Locate and identify every blood parasite.
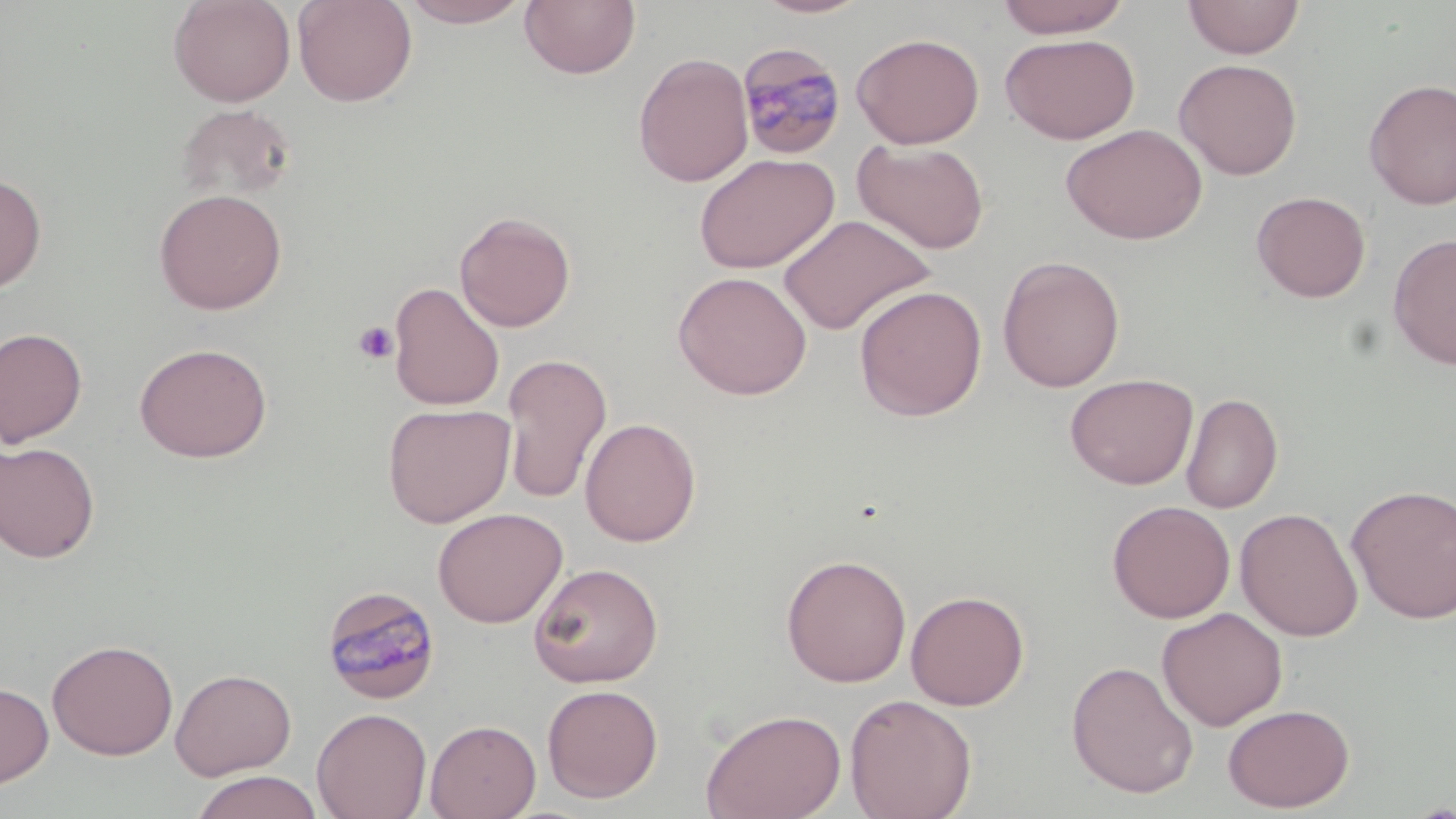

Approximate bounding boxes as named x1/y1/x2/y2 corners in pixels.
Plasmodium malariae-infected red blood cells: (x1=736, y1=42, x2=847, y2=161), (x1=321, y1=585, x2=440, y2=705).
No Plasmodium falciparum, Plasmodium ovale, Plasmodium vivax, Babesia divergens, or Trypanosoma brucei observed.

Summary:
  - Platelet locations: (x1=352, y1=320, x2=398, y2=365)
  - Uninfected red blood cell locations: (x1=168, y1=0, x2=296, y2=106), (x1=292, y1=0, x2=418, y2=107), (x1=398, y1=0, x2=534, y2=28), (x1=519, y1=0, x2=640, y2=80), (x1=752, y1=0, x2=874, y2=19), (x1=994, y1=0, x2=1132, y2=39), (x1=1182, y1=0, x2=1305, y2=59), (x1=851, y1=32, x2=985, y2=149), (x1=1000, y1=34, x2=1140, y2=145), (x1=633, y1=52, x2=754, y2=187), (x1=1174, y1=59, x2=1302, y2=180), (x1=1363, y1=78, x2=1456, y2=210), (x1=175, y1=103, x2=298, y2=204), (x1=1060, y1=123, x2=1208, y2=245), (x1=852, y1=139, x2=990, y2=255), (x1=694, y1=153, x2=839, y2=273), (x1=0, y1=173, x2=47, y2=295), (x1=153, y1=188, x2=287, y2=315), (x1=1251, y1=190, x2=1371, y2=302), (x1=454, y1=210, x2=576, y2=332), (x1=777, y1=214, x2=934, y2=335), (x1=1387, y1=232, x2=1456, y2=370), (x1=996, y1=255, x2=1126, y2=392), (x1=672, y1=271, x2=812, y2=400), (x1=388, y1=281, x2=505, y2=411), (x1=854, y1=285, x2=987, y2=421), (x1=0, y1=327, x2=88, y2=448), (x1=133, y1=342, x2=273, y2=463), (x1=500, y1=353, x2=613, y2=505), (x1=1064, y1=373, x2=1198, y2=490), (x1=1181, y1=392, x2=1283, y2=514), (x1=383, y1=403, x2=514, y2=527), (x1=580, y1=416, x2=701, y2=546), (x1=0, y1=441, x2=101, y2=563), (x1=1346, y1=484, x2=1456, y2=624), (x1=1107, y1=500, x2=1235, y2=623), (x1=433, y1=507, x2=567, y2=628), (x1=1235, y1=507, x2=1363, y2=641), (x1=780, y1=553, x2=912, y2=687), (x1=528, y1=562, x2=663, y2=687), (x1=905, y1=589, x2=1030, y2=710), (x1=1156, y1=607, x2=1287, y2=730), (x1=47, y1=638, x2=178, y2=760), (x1=1065, y1=660, x2=1199, y2=799), (x1=170, y1=668, x2=296, y2=780), (x1=0, y1=681, x2=54, y2=788), (x1=542, y1=683, x2=663, y2=803), (x1=844, y1=693, x2=977, y2=819), (x1=1222, y1=703, x2=1355, y2=813), (x1=427, y1=706, x2=665, y2=810), (x1=311, y1=707, x2=432, y2=819), (x1=700, y1=707, x2=847, y2=819), (x1=425, y1=718, x2=541, y2=819), (x1=188, y1=770, x2=324, y2=819)
  - Slide-level diagnosis: Plasmodium malariae
  - Stain: May-Grünwald-Giemsa
  - Field of view: one of a larger specimen
  - Image size: 1456×819 pixels
  - Magnification: 1000x
  - Preparation: thin blood film
  - Modality: optical microscopy